Classify this cell by malaria status.
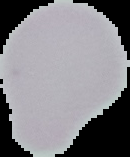

Uninfected.

Summary:
  - Image size: 130×157 pixels
  - Preparation: thin blood film
  - Image type: segmented cell region on a black background